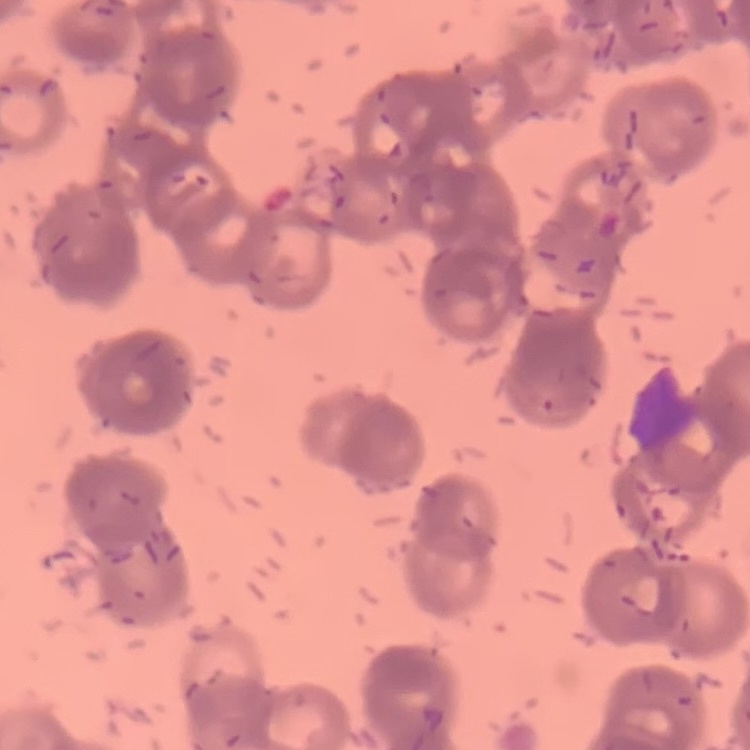

Summary:
  - Red blood cell morphology: rouleaux formation
  - Image type: square crop of a larger photomicrograph
  - Preparation: thin blood film
  - Stain: Field's or Giemsa